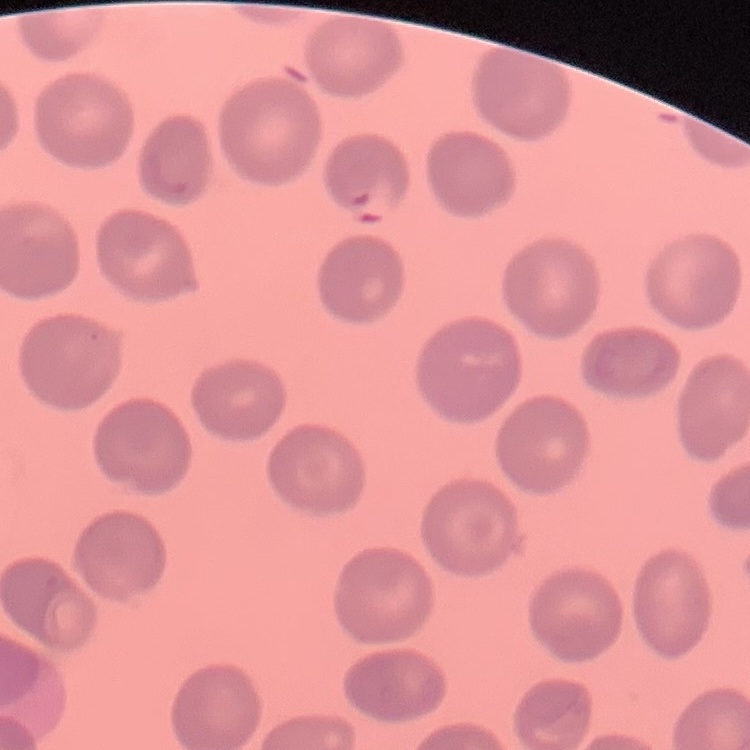

erythrocyte morphology = no rouleaux formation
stain = Field's or Giemsa
preparation = thin peripheral smear
image type = square crop of a larger photomicrograph